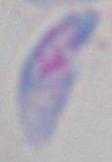

1000x magnification. Micrograph. Toxoplasma gondii is seen.